Comment on the morphology of the red blood cells.
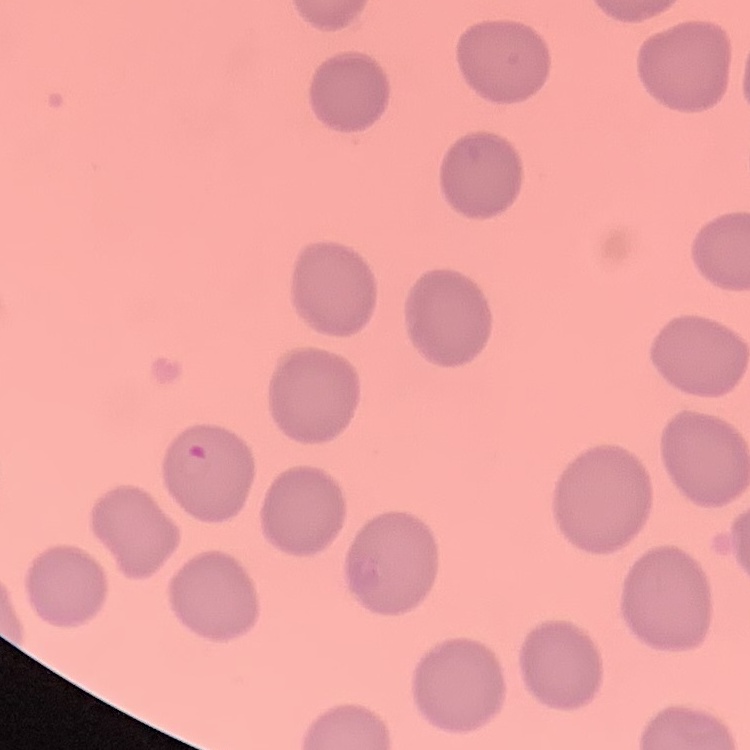
No rouleaux formation.

{
  "image_type": "square crop of a larger photomicrograph",
  "stain": "Field's or Giemsa",
  "preparation": "thin blood film"
}